Assess the morphology of the red blood cells.
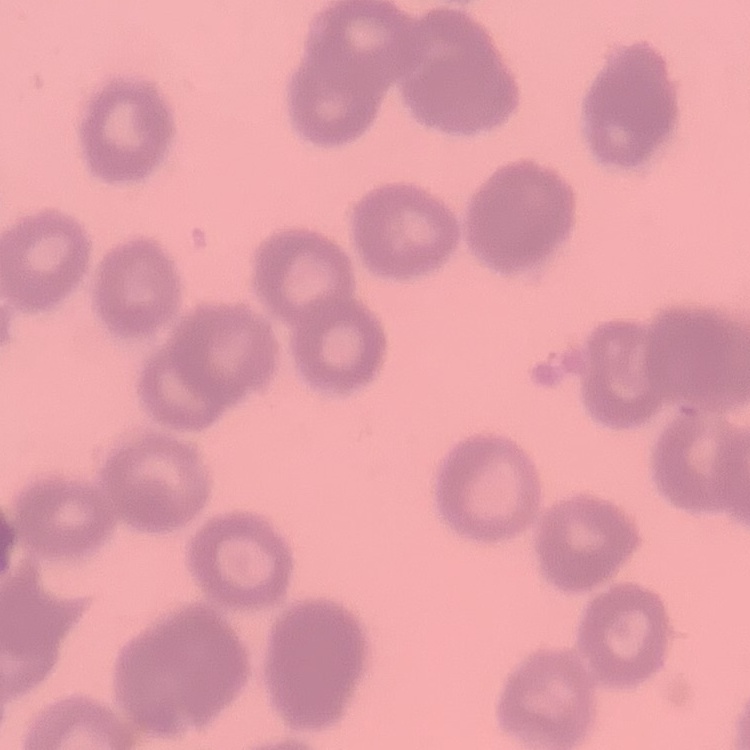
Rouleaux formation.

Summary:
  - Stain: Field's or Giemsa
  - Preparation: thin blood smear
  - Image type: square crop of a larger photomicrograph